Outline each blood parasite and name the species.
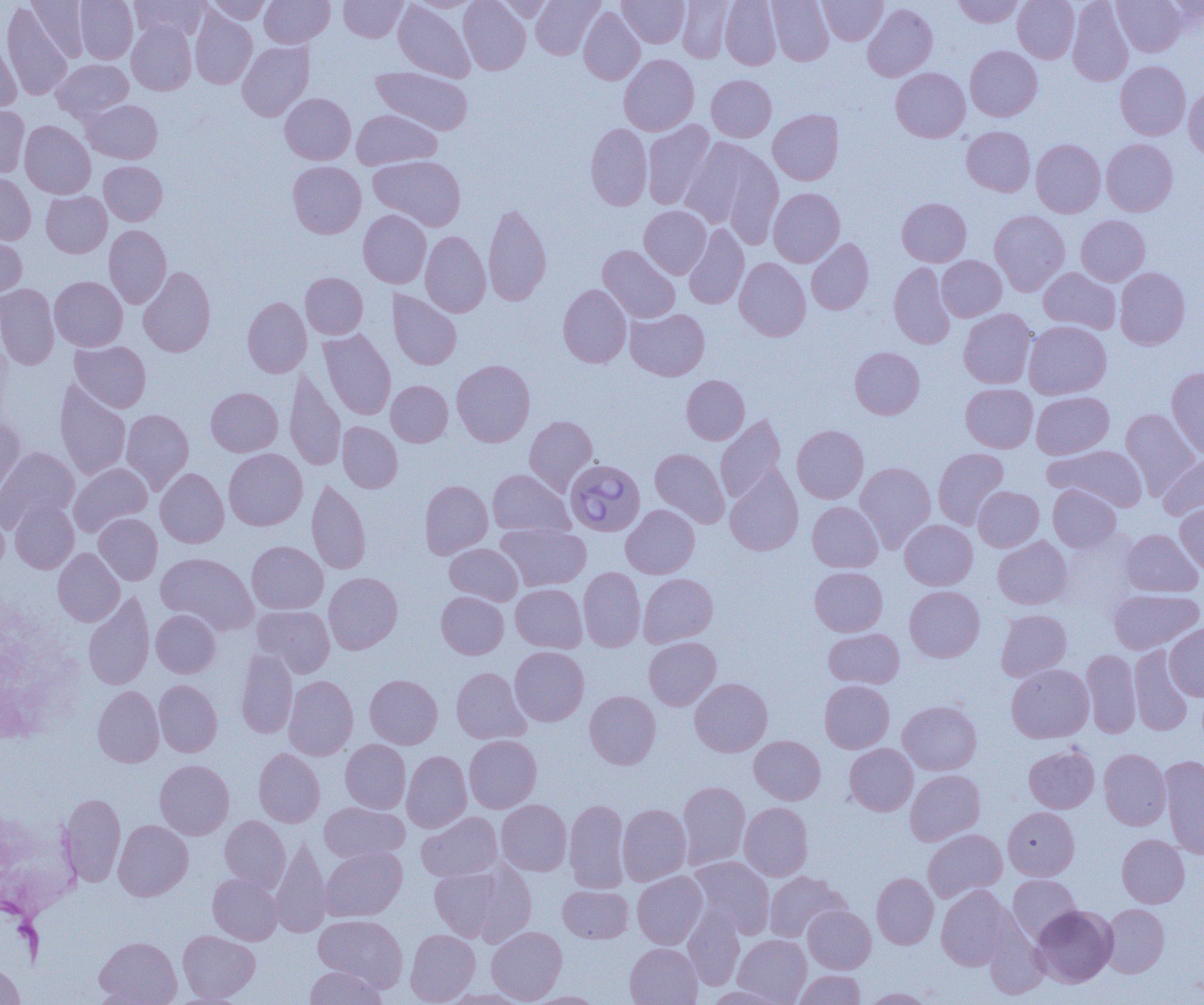

Approximate bounding boxes as named x1/y1/x2/y2 corners in pixels.
Babesia divergens-infected red blood cells: (x1=565, y1=458, x2=646, y2=536).
No Plasmodium falciparum, Plasmodium ovale, Plasmodium malariae, Plasmodium vivax, or Trypanosoma brucei observed.

slide-level diagnosis = Babesia divergens
image size = 1204×1005 pixels
magnification = 1000x
preparation = thin blood smear
field of view = one of a larger specimen
uninfected red blood cell locations = approximate bounding boxes as named x1/y1/x2/y2 corners in pixels: (x1=27, y1=0, x2=90, y2=61), (x1=75, y1=0, x2=137, y2=63), (x1=129, y1=0, x2=208, y2=41), (x1=205, y1=0, x2=272, y2=24), (x1=260, y1=0, x2=335, y2=48), (x1=338, y1=0, x2=407, y2=42), (x1=411, y1=0, x2=480, y2=12), (x1=458, y1=0, x2=530, y2=75), (x1=495, y1=0, x2=556, y2=21), (x1=531, y1=0, x2=604, y2=59), (x1=618, y1=0, x2=689, y2=48), (x1=678, y1=0, x2=734, y2=62), (x1=720, y1=0, x2=782, y2=70), (x1=768, y1=0, x2=833, y2=66), (x1=818, y1=0, x2=887, y2=45), (x1=953, y1=0, x2=1025, y2=28), (x1=1012, y1=0, x2=1079, y2=63), (x1=1067, y1=0, x2=1134, y2=86), (x1=1112, y1=0, x2=1187, y2=56), (x1=393, y1=1, x2=474, y2=82), (x1=1, y1=2, x2=72, y2=100), (x1=1160, y1=2, x2=1204, y2=32), (x1=863, y1=3, x2=938, y2=81), (x1=190, y1=7, x2=257, y2=89), (x1=578, y1=7, x2=645, y2=85), (x1=127, y1=21, x2=196, y2=95), (x1=0, y1=33, x2=21, y2=112), (x1=237, y1=41, x2=314, y2=121), (x1=965, y1=46, x2=1042, y2=121), (x1=619, y1=54, x2=699, y2=135), (x1=52, y1=59, x2=133, y2=121), (x1=1115, y1=61, x2=1191, y2=140), (x1=371, y1=66, x2=473, y2=135), (x1=890, y1=67, x2=970, y2=142), (x1=706, y1=75, x2=776, y2=142), (x1=1183, y1=87, x2=1204, y2=161), (x1=280, y1=93, x2=356, y2=164), (x1=82, y1=99, x2=162, y2=164), (x1=0, y1=104, x2=29, y2=177), (x1=352, y1=109, x2=441, y2=169), (x1=768, y1=109, x2=843, y2=185), (x1=642, y1=120, x2=715, y2=209), (x1=19, y1=121, x2=95, y2=199), (x1=585, y1=123, x2=652, y2=211), (x1=961, y1=126, x2=1035, y2=196), (x1=679, y1=136, x2=776, y2=233), (x1=1101, y1=138, x2=1178, y2=216), (x1=1031, y1=139, x2=1105, y2=217), (x1=369, y1=155, x2=466, y2=231), (x1=99, y1=161, x2=167, y2=225), (x1=287, y1=161, x2=366, y2=238), (x1=0, y1=172, x2=35, y2=245), (x1=768, y1=188, x2=845, y2=267), (x1=41, y1=191, x2=112, y2=257), (x1=897, y1=198, x2=971, y2=266), (x1=483, y1=201, x2=552, y2=306), (x1=639, y1=206, x2=711, y2=278), (x1=358, y1=209, x2=431, y2=288), (x1=989, y1=210, x2=1070, y2=296), (x1=1076, y1=215, x2=1150, y2=286), (x1=683, y1=224, x2=749, y2=309), (x1=104, y1=225, x2=171, y2=309), (x1=420, y1=231, x2=491, y2=317), (x1=0, y1=235, x2=27, y2=297), (x1=806, y1=238, x2=874, y2=314), (x1=598, y1=245, x2=680, y2=323), (x1=936, y1=256, x2=1006, y2=321), (x1=734, y1=257, x2=811, y2=341), (x1=888, y1=263, x2=956, y2=348), (x1=138, y1=266, x2=216, y2=357), (x1=1038, y1=267, x2=1121, y2=334), (x1=1115, y1=268, x2=1190, y2=349), (x1=301, y1=272, x2=368, y2=339), (x1=50, y1=276, x2=128, y2=351), (x1=0, y1=284, x2=59, y2=369), (x1=558, y1=284, x2=632, y2=368), (x1=388, y1=289, x2=462, y2=370), (x1=242, y1=296, x2=311, y2=377), (x1=625, y1=308, x2=710, y2=381), (x1=959, y1=309, x2=1038, y2=389), (x1=1023, y1=321, x2=1111, y2=399), (x1=318, y1=329, x2=396, y2=419), (x1=0, y1=331, x2=12, y2=421), (x1=70, y1=341, x2=151, y2=412), (x1=850, y1=347, x2=925, y2=419), (x1=452, y1=359, x2=535, y2=446), (x1=1166, y1=367, x2=1204, y2=459), (x1=285, y1=369, x2=346, y2=470), (x1=681, y1=375, x2=750, y2=444), (x1=54, y1=379, x2=131, y2=481), (x1=386, y1=380, x2=453, y2=446), (x1=961, y1=383, x2=1038, y2=452), (x1=206, y1=387, x2=282, y2=456), (x1=1031, y1=391, x2=1114, y2=459), (x1=1121, y1=408, x2=1201, y2=499), (x1=121, y1=409, x2=193, y2=494), (x1=715, y1=414, x2=787, y2=504), (x1=524, y1=415, x2=598, y2=494), (x1=0, y1=418, x2=25, y2=500), (x1=337, y1=422, x2=402, y2=493), (x1=792, y1=425, x2=868, y2=503), (x1=1045, y1=445, x2=1148, y2=511), (x1=0, y1=447, x2=79, y2=531), (x1=224, y1=448, x2=307, y2=530), (x1=650, y1=448, x2=729, y2=528), (x1=933, y1=448, x2=1009, y2=529), (x1=1158, y1=456, x2=1204, y2=520), (x1=69, y1=462, x2=153, y2=536), (x1=855, y1=462, x2=936, y2=550), (x1=155, y1=468, x2=229, y2=548), (x1=725, y1=468, x2=804, y2=556), (x1=488, y1=469, x2=573, y2=538), (x1=306, y1=479, x2=371, y2=574), (x1=419, y1=480, x2=493, y2=559), (x1=1047, y1=484, x2=1121, y2=552), (x1=973, y1=486, x2=1044, y2=551), (x1=10, y1=500, x2=79, y2=573), (x1=807, y1=501, x2=882, y2=572), (x1=1175, y1=503, x2=1204, y2=575), (x1=0, y1=505, x2=9, y2=577), (x1=621, y1=505, x2=700, y2=578), (x1=94, y1=513, x2=162, y2=585), (x1=900, y1=519, x2=977, y2=590), (x1=496, y1=523, x2=592, y2=591), (x1=1121, y1=529, x2=1202, y2=597), (x1=993, y1=536, x2=1072, y2=609), (x1=247, y1=541, x2=328, y2=614), (x1=444, y1=543, x2=523, y2=605), (x1=53, y1=548, x2=124, y2=626), (x1=156, y1=552, x2=258, y2=634), (x1=810, y1=566, x2=887, y2=636), (x1=578, y1=567, x2=645, y2=651), (x1=324, y1=572, x2=402, y2=654), (x1=638, y1=573, x2=718, y2=647), (x1=511, y1=584, x2=588, y2=653), (x1=904, y1=585, x2=985, y2=662), (x1=1108, y1=589, x2=1203, y2=654), (x1=436, y1=591, x2=508, y2=659), (x1=83, y1=592, x2=154, y2=690), (x1=252, y1=605, x2=334, y2=677), (x1=151, y1=609, x2=220, y2=677), (x1=996, y1=609, x2=1072, y2=681), (x1=1166, y1=623, x2=1204, y2=699), (x1=824, y1=628, x2=904, y2=689), (x1=644, y1=636, x2=721, y2=710), (x1=510, y1=646, x2=589, y2=726), (x1=1130, y1=646, x2=1194, y2=735), (x1=235, y1=649, x2=298, y2=738), (x1=1082, y1=649, x2=1141, y2=738), (x1=1007, y1=664, x2=1093, y2=743), (x1=451, y1=667, x2=531, y2=744), (x1=365, y1=674, x2=442, y2=748), (x1=284, y1=675, x2=358, y2=760), (x1=690, y1=678, x2=773, y2=756), (x1=154, y1=680, x2=222, y2=757), (x1=820, y1=680, x2=894, y2=753), (x1=93, y1=685, x2=164, y2=767), (x1=585, y1=690, x2=661, y2=769), (x1=898, y1=700, x2=981, y2=775), (x1=464, y1=735, x2=542, y2=813), (x1=749, y1=735, x2=826, y2=804), (x1=340, y1=739, x2=411, y2=813), (x1=845, y1=743, x2=918, y2=815), (x1=1024, y1=745, x2=1099, y2=813), (x1=253, y1=748, x2=325, y2=827), (x1=1099, y1=749, x2=1170, y2=830), (x1=402, y1=750, x2=472, y2=832), (x1=1158, y1=755, x2=1204, y2=858), (x1=155, y1=760, x2=234, y2=840), (x1=905, y1=769, x2=985, y2=845), (x1=678, y1=781, x2=750, y2=869), (x1=58, y1=793, x2=126, y2=887), (x1=496, y1=800, x2=572, y2=876), (x1=564, y1=800, x2=629, y2=893), (x1=319, y1=802, x2=409, y2=863), (x1=739, y1=802, x2=813, y2=880), (x1=617, y1=803, x2=691, y2=885), (x1=1003, y1=807, x2=1079, y2=880), (x1=417, y1=811, x2=502, y2=882), (x1=220, y1=815, x2=290, y2=892), (x1=113, y1=820, x2=193, y2=901), (x1=923, y1=829, x2=1007, y2=902), (x1=1117, y1=834, x2=1189, y2=907), (x1=270, y1=839, x2=332, y2=937), (x1=321, y1=846, x2=407, y2=921), (x1=689, y1=856, x2=774, y2=939), (x1=429, y1=864, x2=531, y2=944), (x1=632, y1=871, x2=707, y2=949), (x1=764, y1=871, x2=848, y2=942), (x1=208, y1=873, x2=282, y2=944), (x1=871, y1=873, x2=938, y2=949), (x1=1008, y1=874, x2=1081, y2=943), (x1=558, y1=885, x2=633, y2=943), (x1=937, y1=885, x2=1015, y2=970), (x1=803, y1=904, x2=876, y2=973), (x1=1101, y1=904, x2=1169, y2=977), (x1=1031, y1=905, x2=1117, y2=987), (x1=683, y1=906, x2=745, y2=990), (x1=314, y1=914, x2=408, y2=991), (x1=983, y1=922, x2=1048, y2=999), (x1=487, y1=926, x2=567, y2=1003), (x1=405, y1=929, x2=480, y2=1004), (x1=178, y1=930, x2=260, y2=1002), (x1=733, y1=935, x2=811, y2=1004), (x1=95, y1=936, x2=181, y2=1004), (x1=625, y1=943, x2=703, y2=1005), (x1=0, y1=962, x2=24, y2=1005), (x1=304, y1=965, x2=386, y2=1005), (x1=794, y1=970, x2=865, y2=1005), (x1=704, y1=986, x2=786, y2=1004), (x1=861, y1=987, x2=936, y2=1004), (x1=441, y1=989, x2=532, y2=1005), (x1=524, y1=991, x2=607, y2=1005)
modality = optical microscopy